Comment on the morphology of the red blood cells.
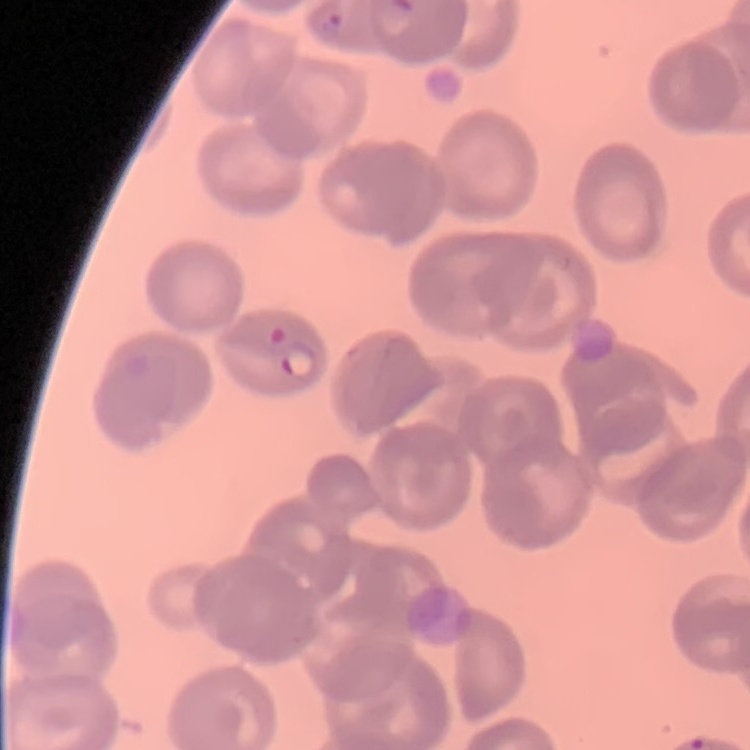
They show no rouleaux formation.

Square crop of a larger photomicrograph. Thin blood film. Stained with either Field's or Giemsa.